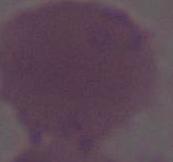
Summary:
  - Magnification: 1000x
  - Modality: micrograph
  - Identification: erythrocyte